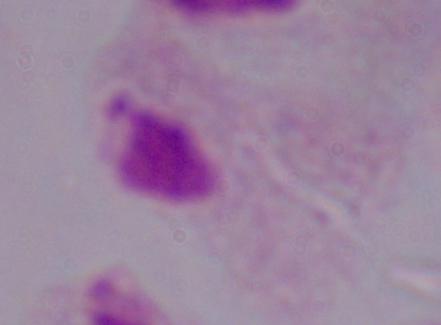
Summary:
  - Modality: micrograph
  - Magnification: 1000x
  - Identification: trichomonad